State which parasite is depicted.
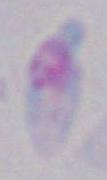
This is Toxoplasma gondii.

Summary:
  - Magnification: 1000x
  - Modality: micrograph